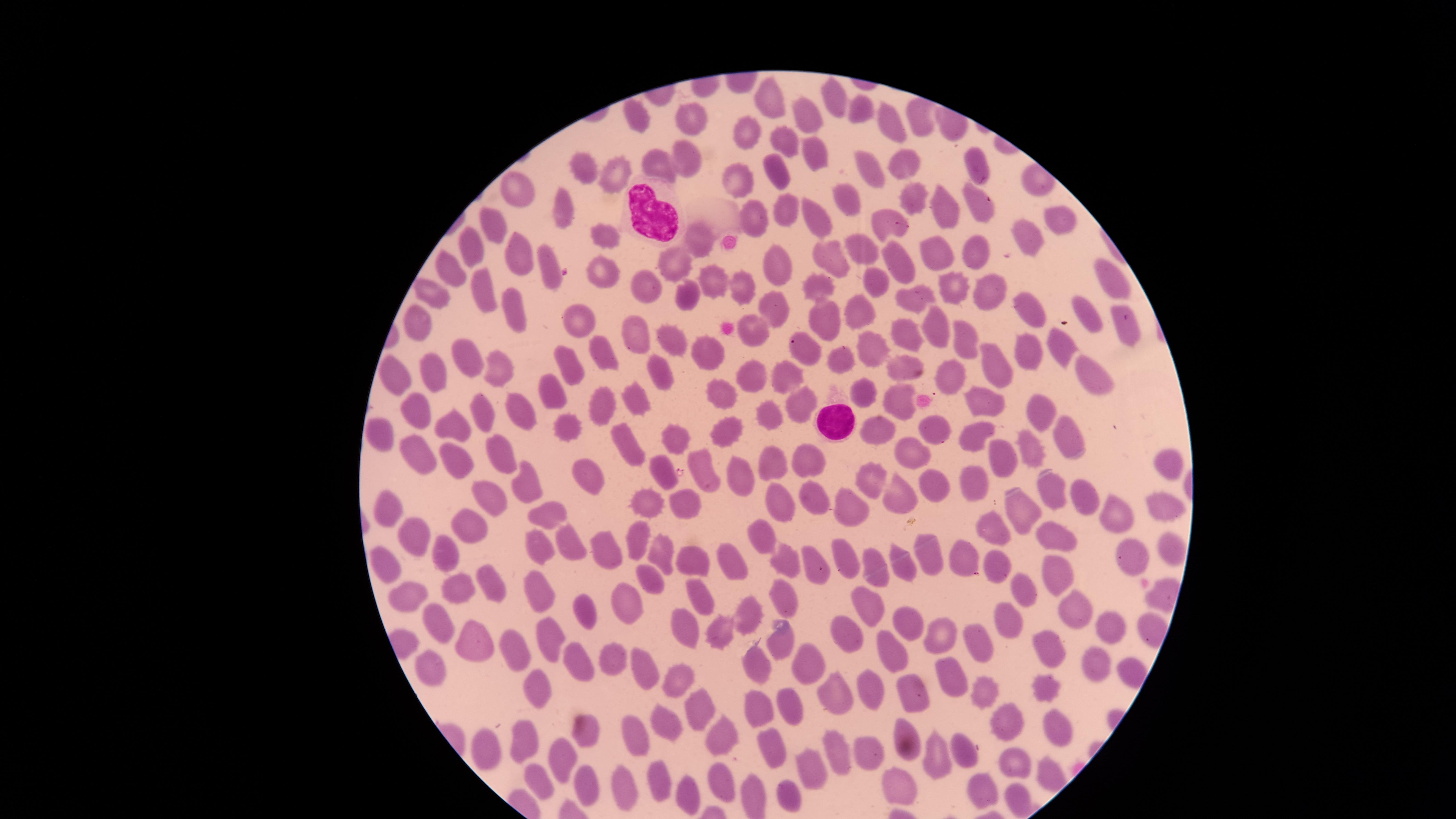
presence: no malaria parasites detected
stain: Giemsa
uninfected_red_blood_cells: 'approximate marker points as [x, y] in pixels: [835, 97], [770, 99], [862, 104], [637, 117], [809, 118], [891, 118], [919, 119], [695, 120], [753, 134], [785, 138], [680, 151], [818, 156], [658, 165], [903, 165], [973, 166], [869, 167], [579, 171], [776, 173], [739, 174], [620, 177], [522, 186], [845, 194], [915, 195], [974, 206], [562, 209], [941, 209], [783, 212], [750, 216], [817, 219], [889, 221], [1063, 221], [495, 231], [599, 235], [1024, 238], [693, 239], [862, 248], [472, 249], [975, 250], [935, 254], [833, 255], [519, 258], [774, 261], [674, 262], [900, 263], [550, 266], [451, 273], [603, 274], [1109, 275], [714, 282], [871, 282], [480, 287], [646, 287], [743, 287], [819, 287], [950, 289], [985, 292], [432, 295], [687, 297], [1024, 299], [917, 301], [774, 306], [863, 306], [519, 314], [1089, 317], [418, 320], [583, 320], [825, 323], [938, 330], [904, 333], [634, 334], [758, 334], [963, 340], [670, 341], [872, 345], [1062, 348], [606, 350], [808, 350], [1026, 350], [708, 354], [468, 355], [846, 359], [900, 364], [497, 366], [391, 367], [572, 368], [997, 369], [431, 370], [1090, 372], [663, 374], [752, 376], [783, 378], [946, 378], [554, 390], [863, 390], [634, 394], [724, 395], [897, 399], [605, 403], [791, 404], [983, 404], [416, 407], [480, 410], [518, 410], [1036, 410], [765, 412], [566, 424], [724, 425], [871, 427], [928, 427], [458, 428], [1070, 429], [380, 433], [678, 434], [976, 437], [623, 439], [1030, 449], [905, 451], [417, 453], [504, 453], [1001, 458], [811, 461], [1164, 461], [450, 462], [660, 468], [774, 468], [740, 473], [704, 474], [869, 479], [591, 480], [931, 485], [1041, 485], [533, 486], [972, 489], [897, 495], [1079, 495], [490, 496], [780, 499], [820, 499], [685, 503], [651, 505], [853, 505], [1161, 505], [1013, 506], [387, 508], [1111, 512], [552, 519], [465, 525], [1054, 527], [995, 528], [762, 533], [415, 535], [640, 541], [531, 545], [1173, 547], [603, 550], [958, 551], [574, 552], [664, 553], [929, 554], [448, 555], [694, 556], [1138, 556], [846, 557], [384, 559], [999, 559], [787, 560], [908, 562], [731, 563], [813, 566], [1055, 566], [879, 568], [647, 580], [488, 582], [535, 582], [1021, 590], [454, 591], [409, 596], [700, 598], [781, 599], [874, 606], [630, 609], [751, 610], [1075, 612], [589, 615], [1014, 622], [443, 624], [910, 625], [1112, 627], [721, 629], [688, 631], [848, 631], [939, 635], [557, 640], [782, 640], [478, 644], [981, 644], [1054, 646], [509, 648], [892, 652], [577, 659], [616, 660], [1105, 662], [758, 668], [427, 669], [812, 670], [648, 672], [677, 680], [949, 680], [866, 688], [1049, 690], [539, 692], [982, 694], [911, 698], [839, 701], [697, 703], [792, 706], [756, 709], [665, 718], [1010, 727], [1060, 727], [582, 730], [904, 730], [642, 732], [725, 736], [523, 738], [483, 742], [770, 746], [834, 750], [964, 751], [868, 753], [562, 756], [940, 761], [1010, 765], [1043, 772], [811, 773], [539, 775], [724, 777], [659, 778], [897, 784], [585, 788], [985, 789], [623, 792], [755, 794], [790, 794], [687, 795], [1019, 801]'
visible_region: circular
preparation: thin blood film
field_of_view: single
white_blood_cells: 'approximate marker points as [x, y] in pixels: [658, 216], [830, 425]'
image_size: 1456×819 pixels
capture: smartphone photograph through the microscope eyepiece